Locate every blood parasite and identify its species.
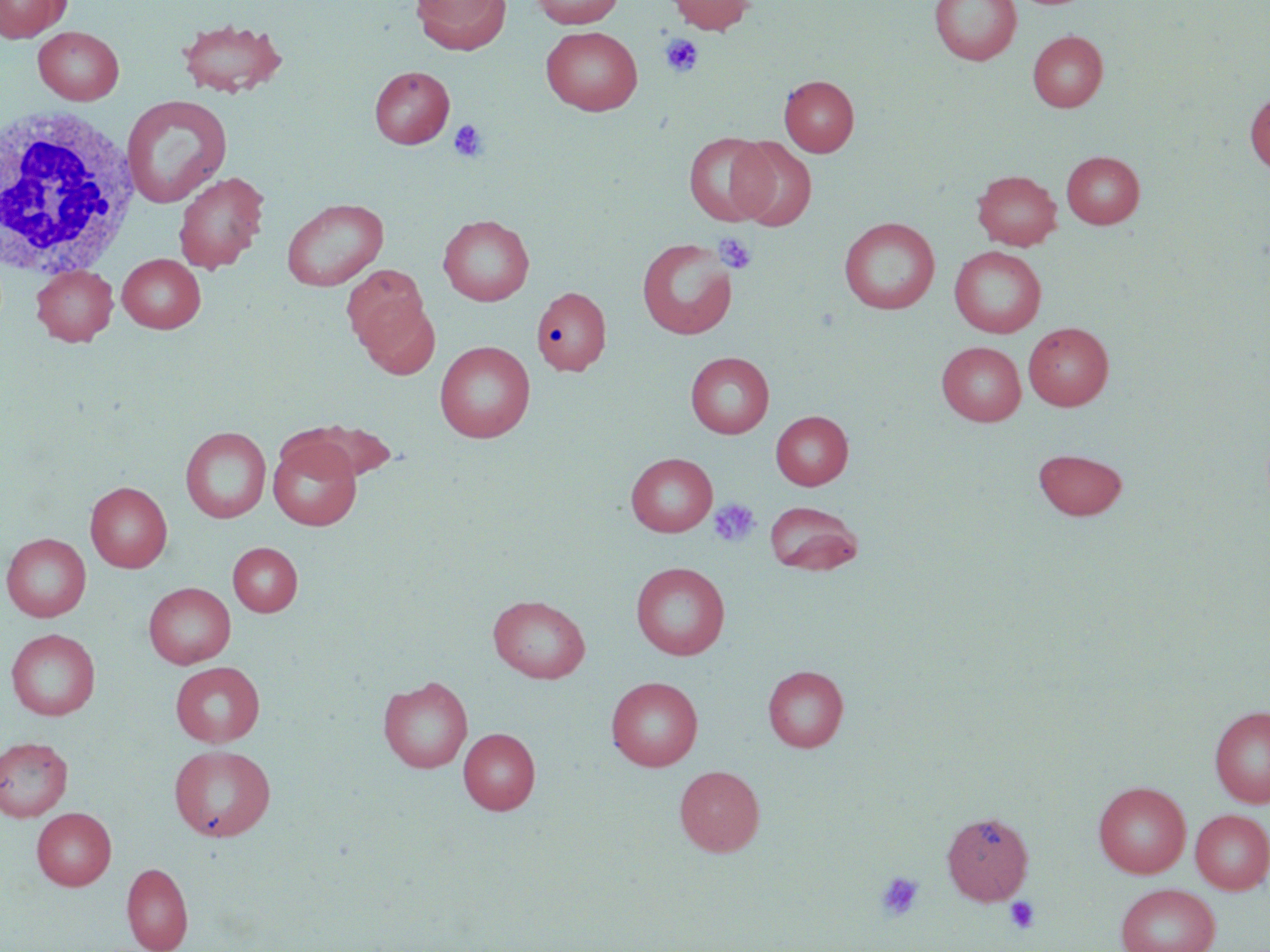
No blood parasites observed.

Approximate bounding boxes as named x1/y1/x2/y2 corners in pixels. White blood cell locations: (x1=1, y1=102, x2=141, y2=281). Platelet locations: (x1=660, y1=34, x2=704, y2=77), (x1=449, y1=119, x2=489, y2=162), (x1=712, y1=232, x2=757, y2=274), (x1=708, y1=498, x2=761, y2=548), (x1=875, y1=871, x2=925, y2=921), (x1=1003, y1=896, x2=1040, y2=933). Uninfected red blood cell locations: (x1=0, y1=0, x2=70, y2=42), (x1=412, y1=0, x2=510, y2=54), (x1=530, y1=0, x2=623, y2=28), (x1=667, y1=0, x2=755, y2=34), (x1=930, y1=0, x2=1020, y2=65), (x1=176, y1=17, x2=288, y2=98), (x1=541, y1=26, x2=643, y2=115), (x1=33, y1=27, x2=124, y2=104), (x1=1027, y1=31, x2=1108, y2=112), (x1=369, y1=66, x2=454, y2=148), (x1=780, y1=75, x2=859, y2=156), (x1=1245, y1=92, x2=1270, y2=176), (x1=122, y1=94, x2=233, y2=209), (x1=684, y1=132, x2=773, y2=227), (x1=729, y1=137, x2=817, y2=231), (x1=1061, y1=151, x2=1145, y2=228), (x1=973, y1=170, x2=1062, y2=250), (x1=174, y1=171, x2=268, y2=274), (x1=281, y1=197, x2=388, y2=291), (x1=438, y1=214, x2=534, y2=306), (x1=839, y1=217, x2=940, y2=314), (x1=637, y1=237, x2=738, y2=340), (x1=949, y1=246, x2=1046, y2=337), (x1=117, y1=253, x2=206, y2=333), (x1=31, y1=265, x2=118, y2=345), (x1=342, y1=265, x2=430, y2=356), (x1=535, y1=281, x2=609, y2=376), (x1=358, y1=299, x2=440, y2=380), (x1=1023, y1=323, x2=1114, y2=410), (x1=434, y1=340, x2=535, y2=443), (x1=937, y1=341, x2=1026, y2=426), (x1=685, y1=352, x2=774, y2=437), (x1=771, y1=411, x2=853, y2=489), (x1=289, y1=419, x2=400, y2=481), (x1=180, y1=426, x2=271, y2=523), (x1=268, y1=436, x2=362, y2=530), (x1=1033, y1=449, x2=1128, y2=520), (x1=625, y1=452, x2=717, y2=537), (x1=85, y1=481, x2=172, y2=572), (x1=764, y1=500, x2=863, y2=576), (x1=1, y1=533, x2=91, y2=622), (x1=228, y1=542, x2=302, y2=616), (x1=630, y1=561, x2=730, y2=660), (x1=143, y1=582, x2=235, y2=668), (x1=488, y1=595, x2=591, y2=683), (x1=5, y1=628, x2=101, y2=720), (x1=170, y1=661, x2=265, y2=747), (x1=763, y1=665, x2=849, y2=752), (x1=377, y1=675, x2=473, y2=773), (x1=606, y1=676, x2=703, y2=770), (x1=1209, y1=705, x2=1270, y2=808), (x1=458, y1=728, x2=540, y2=814), (x1=0, y1=737, x2=73, y2=821), (x1=169, y1=744, x2=276, y2=841), (x1=675, y1=765, x2=765, y2=856), (x1=1093, y1=781, x2=1190, y2=878), (x1=31, y1=807, x2=116, y2=890), (x1=1190, y1=809, x2=1270, y2=894), (x1=942, y1=811, x2=1034, y2=905), (x1=122, y1=862, x2=193, y2=952), (x1=1115, y1=883, x2=1220, y2=952). Slide-level diagnosis: negative for blood parasites. Image is 1270×952 pixels. Optical microscopy. One field of a larger specimen. 1000x magnification. May-Grünwald-Giemsa-stained preparation. Thin blood smear.